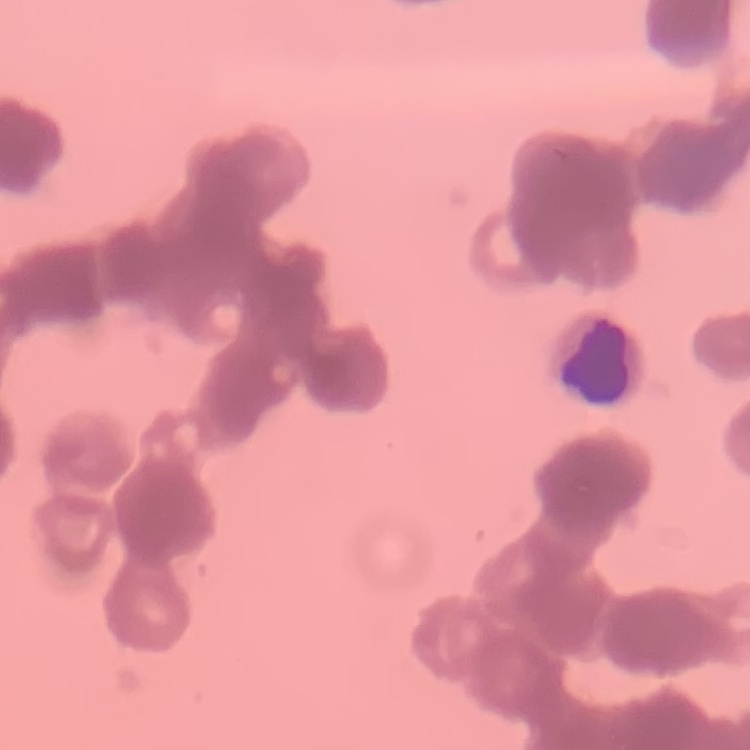

The red blood cells show rouleaux formation. Square crop of a larger photomicrograph. Field's or Giemsa stain. Thin peripheral smear.